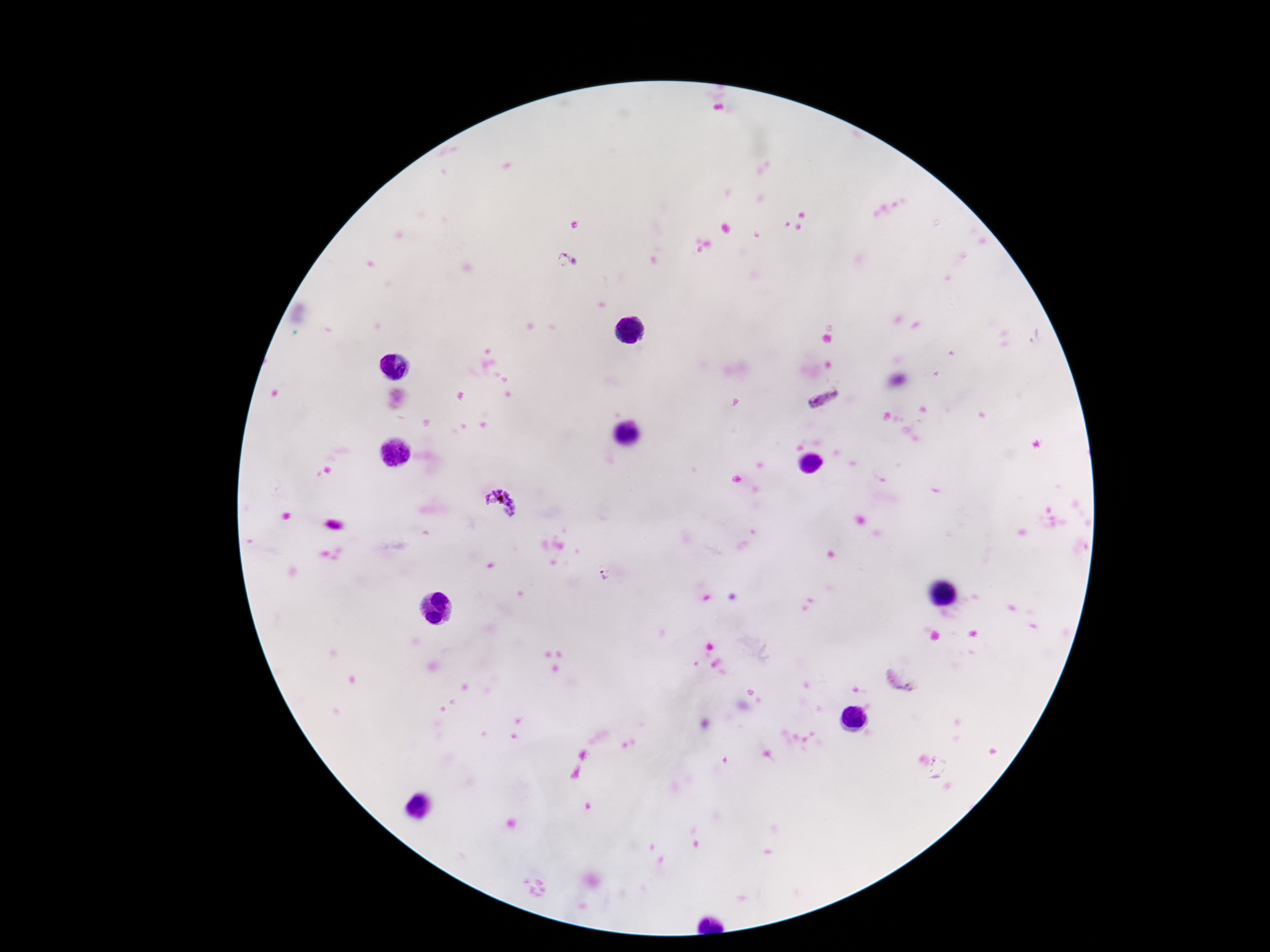
Approximate object centers, in pixels from the top-left corner.
Summary:
  - Plasmodium parasite locations: (x=566, y=261), (x=824, y=399), (x=500, y=504), (x=903, y=676)
  - Patient malaria status: positive
  - Magnification: 100x
  - Preparation: thick blood smear
  - Image size: 1270×952 pixels
  - Stain: Giemsa
  - Capture: smartphone camera through the microscope eyepiece
  - Field of view: one from this slide